Assess this cell for malaria.
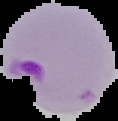

Parasitized.

Image is 118×121 pixels. Cell region segmented out of the field of view; the surrounding area is masked to black. From a thin blood film.